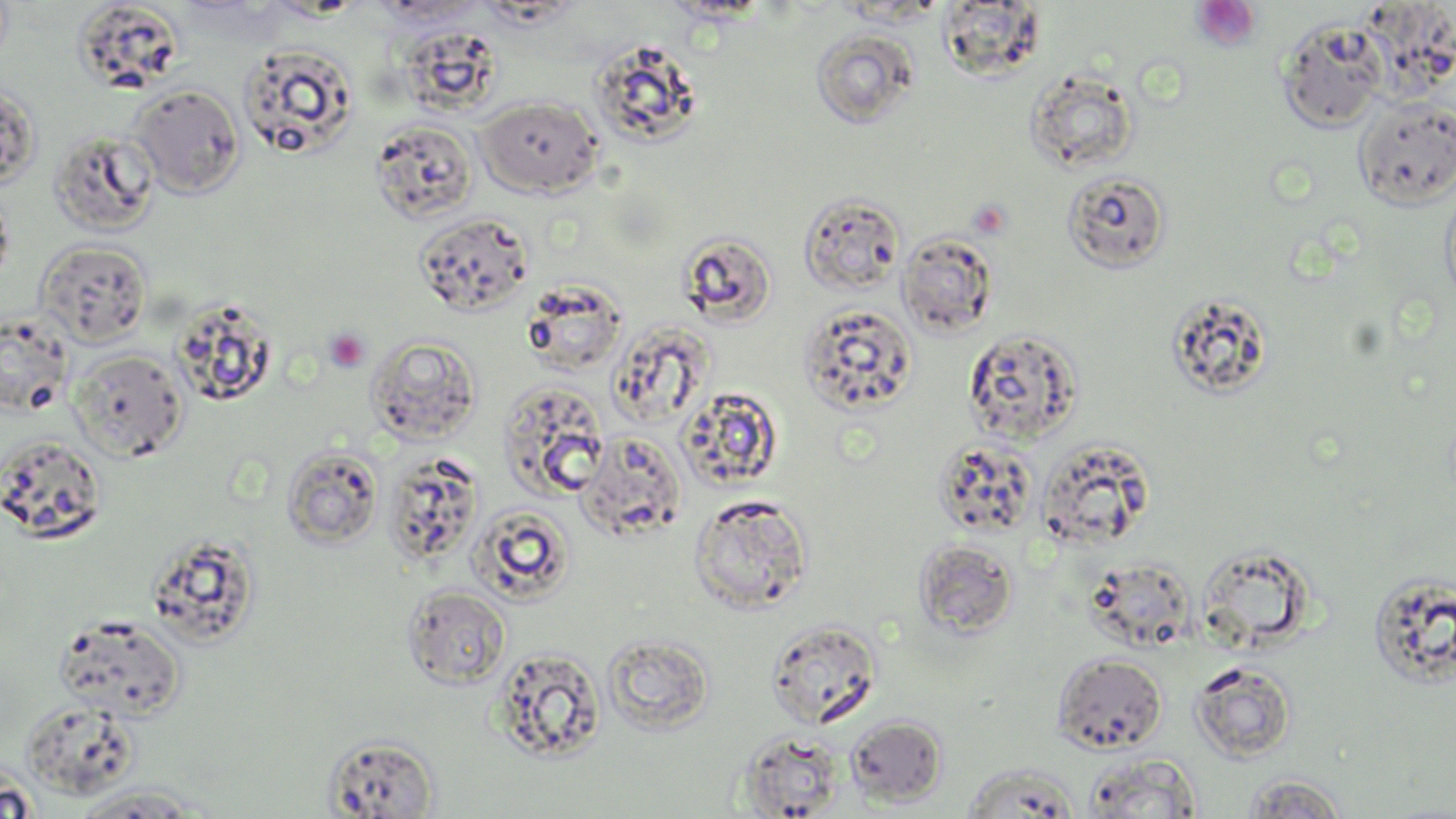
slide-level diagnosis = no evidence of blood parasites
uninfected red blood cell locations = approximate bounding boxes as (x1,y1)-(x2,y2) corner pairs in pixels: (72,0)-(193,93), (936,2)-(1048,81), (1277,18)-(1388,133), (395,26)-(507,121), (810,27)-(919,128), (589,42)-(702,157), (237,43)-(359,159), (1025,67)-(1139,174), (0,80)-(40,190), (128,84)-(245,198), (476,96)-(603,198), (1353,97)-(1456,209), (369,120)-(478,223), (48,129)-(160,237), (1063,171)-(1170,273), (1441,177)-(1456,314), (0,185)-(15,289), (798,192)-(906,295), (414,212)-(534,317), (677,231)-(778,328), (897,232)-(998,339), (35,239)-(151,348), (520,278)-(627,377), (1166,293)-(1274,400), (171,300)-(279,406), (798,303)-(918,416), (0,314)-(73,417), (607,314)-(720,424), (963,328)-(1083,445), (365,334)-(482,446), (68,348)-(188,462), (497,380)-(610,500), (676,388)-(776,493), (576,433)-(686,541), (0,434)-(108,544), (933,438)-(1039,540), (1035,438)-(1157,551), (281,445)-(383,549), (382,452)-(484,570), (689,493)-(813,614), (469,504)-(576,604), (146,535)-(262,646), (913,539)-(1019,640), (1195,549)-(1315,652), (1085,559)-(1196,652), (1367,571)-(1456,688), (403,584)-(511,689), (53,615)-(186,721), (766,619)-(882,730), (602,633)-(715,735), (491,647)-(606,762), (1052,653)-(1167,754), (1189,660)-(1298,763), (19,700)-(140,800), (847,715)-(948,807), (739,730)-(845,817), (323,733)-(440,817), (1082,752)-(1204,818), (961,765)-(1082,817), (0,773)-(38,819), (1240,774)-(1349,819), (67,784)-(211,816)
platelet locations = approximate bounding boxes as (x1,y1)-(x2,y2) corner pairs in pixels: (1191,1)-(1260,51), (967,199)-(1012,240), (323,329)-(370,373)
modality = optical microscopy
field of view = one of a larger specimen
stain = May-Grünwald-Giemsa
image size = 1456×819 pixels
magnification = 1000x
preparation = thin blood film